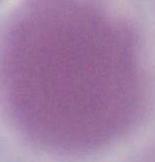

identification = erythrocyte
modality = photomicrograph
magnification = 1000x